Give the extent of all Plasmodium vivax-infected red blood cells.
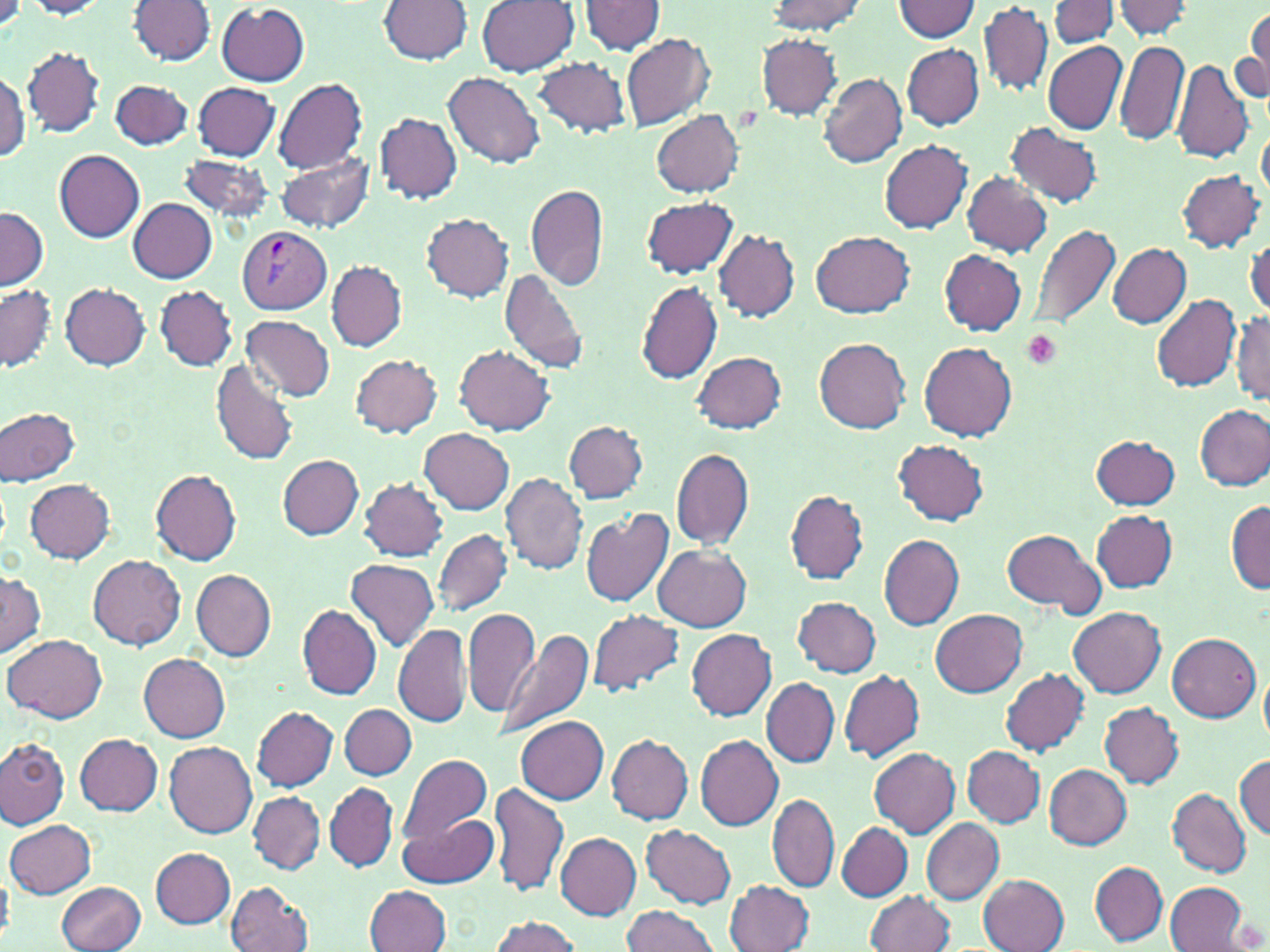
Approximate bounding boxes as (x1,y1)-(x2,y2) corner pairs in pixels.
Plasmodium vivax-infected red blood cells: (238,226)-(332,313).

slide-level diagnosis = Plasmodium vivax
uninfected red blood cell locations = approximate bounding boxes as (x1,y1)-(x2,y2) corner pairs in pixels: (767,0)-(865,34), (1050,0)-(1119,49), (1112,0)-(1197,39), (23,1)-(112,19), (129,1)-(216,64), (378,1)-(472,65), (477,1)-(579,76), (891,1)-(981,41), (578,2)-(668,57), (217,3)-(310,85), (979,3)-(1053,97), (1242,11)-(1270,104), (621,32)-(715,131), (756,33)-(844,118), (1115,40)-(1189,146), (1043,41)-(1127,135), (902,45)-(984,130), (23,46)-(105,136), (531,57)-(631,137), (1170,58)-(1255,163), (0,72)-(29,162), (445,73)-(545,167), (819,74)-(907,167), (109,79)-(194,149), (272,79)-(368,177), (192,83)-(279,160), (651,109)-(744,196), (375,114)-(462,203), (1005,123)-(1104,208), (1257,123)-(1269,208), (880,140)-(973,233), (54,150)-(145,242), (277,151)-(375,236), (177,154)-(275,224), (1178,170)-(1265,252), (963,173)-(1052,256), (526,182)-(609,291), (641,195)-(736,277), (129,199)-(216,282), (1,205)-(48,291), (422,213)-(514,301), (1030,222)-(1122,335), (715,230)-(799,323), (812,231)-(916,318), (1246,234)-(1270,319), (1107,243)-(1191,328), (938,250)-(1027,333), (328,261)-(408,350), (499,269)-(592,375), (636,281)-(723,384), (60,282)-(150,369), (1,284)-(57,372), (155,285)-(237,370), (1152,295)-(1241,391), (1233,310)-(1270,404), (242,315)-(335,402), (814,338)-(910,434), (919,342)-(1018,440), (456,345)-(555,434), (692,351)-(788,433), (351,354)-(442,437), (210,360)-(299,468), (1195,406)-(1270,491), (1,407)-(80,485), (564,420)-(647,503), (421,428)-(514,514), (1090,435)-(1181,510), (894,439)-(988,525), (670,448)-(754,549), (278,454)-(364,541), (151,469)-(241,565), (501,473)-(589,575), (25,477)-(116,562), (360,478)-(447,561), (784,489)-(870,585), (1226,502)-(1270,591), (581,509)-(674,608), (1091,510)-(1178,592), (999,527)-(1106,618), (433,530)-(512,617), (879,533)-(965,629), (656,546)-(752,631), (88,554)-(185,649), (345,558)-(439,653), (191,568)-(275,659), (0,569)-(44,656), (792,596)-(881,677), (297,604)-(382,701), (462,608)-(540,718), (588,608)-(685,697), (1069,608)-(1166,698), (932,609)-(1027,697), (393,624)-(472,728), (494,627)-(595,738), (686,629)-(778,720), (1167,632)-(1261,721), (5,633)-(108,722), (139,652)-(231,740), (1001,668)-(1089,756), (1261,668)-(1270,749), (838,670)-(924,762), (761,678)-(839,768), (1099,702)-(1184,788), (340,704)-(417,778), (251,706)-(339,791), (515,713)-(608,804), (73,733)-(163,815), (608,734)-(692,824), (696,734)-(782,830), (0,738)-(70,829), (164,740)-(257,838), (963,746)-(1045,827), (869,747)-(960,836), (397,752)-(494,847), (1234,755)-(1269,838), (1043,763)-(1131,849), (489,779)-(568,898), (324,783)-(397,873), (1167,788)-(1252,877), (249,792)-(325,874), (767,794)-(839,892), (398,810)-(498,888), (921,818)-(1004,905), (5,820)-(95,899), (837,823)-(912,902), (643,825)-(736,907), (556,832)-(642,920), (151,848)-(236,927), (1091,862)-(1167,945), (0,867)-(13,944), (979,873)-(1069,952), (725,879)-(813,952), (57,880)-(147,952), (227,880)-(313,952), (1166,882)-(1250,952), (366,885)-(451,952), (866,890)-(955,952), (621,905)-(721,952), (488,915)-(582,952)
modality = light microscopy
preparation = thin blood smear
platelet locations = approximate bounding boxes as (x1,y1)-(x2,y2) corner pairs in pixels: (1022,331)-(1063,370)
image size = 1270×952 pixels
stain = May-Grünwald-Giemsa
magnification = 1000x
field of view = one of a larger specimen